Locate every Plasmodium falciparum-infected red blood cell.
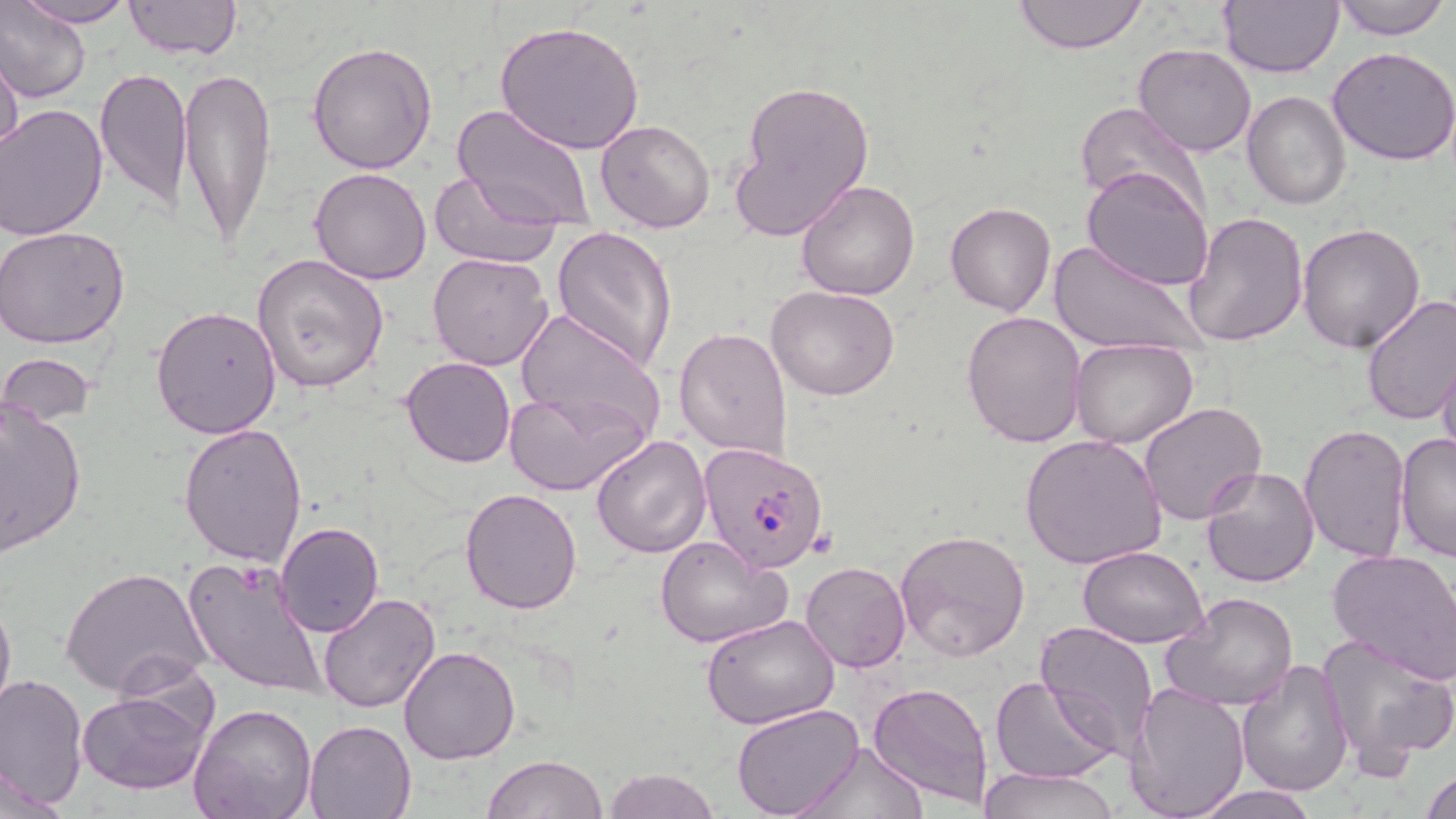
Approximate bounding boxes as [x1, y1, x2, y2] in pixels.
Plasmodium falciparum-infected red blood cells: [698, 439, 832, 572].

slide-level diagnosis = Plasmodium falciparum
modality = light microscopy
image size = 1456×819 pixels
stain = May-Grünwald-Giemsa
field of view = single
uninfected red blood cell locations = approximate bounding boxes as [x1, y1, x2, y2] in pixels: [0, 0, 91, 105], [1015, 0, 1148, 52], [1332, 0, 1451, 40], [15, 1, 136, 27], [122, 1, 243, 59], [1218, 1, 1343, 77], [495, 20, 644, 157], [308, 41, 440, 176], [1133, 42, 1256, 157], [0, 46, 23, 167], [1328, 46, 1456, 166], [178, 64, 279, 250], [95, 66, 193, 213], [729, 78, 875, 240], [1243, 91, 1351, 209], [1072, 100, 1207, 216], [452, 103, 598, 232], [1, 104, 109, 242], [595, 119, 716, 233], [310, 166, 433, 283], [1083, 167, 1214, 294], [432, 169, 563, 271], [795, 179, 922, 300], [945, 202, 1055, 317], [1182, 210, 1310, 347], [1297, 224, 1426, 352], [0, 226, 131, 348], [553, 226, 678, 370], [1047, 239, 1204, 355], [428, 252, 554, 371], [251, 254, 390, 394], [767, 284, 900, 401], [1359, 294, 1456, 425], [690, 304, 891, 427], [151, 306, 280, 438], [512, 307, 666, 444], [961, 309, 1088, 448], [674, 327, 794, 458], [1069, 337, 1199, 449], [1436, 352, 1456, 464], [0, 354, 98, 429], [400, 357, 516, 467], [504, 388, 646, 497], [0, 400, 87, 557], [1138, 402, 1268, 524], [178, 422, 307, 566], [1299, 423, 1410, 564], [1394, 431, 1456, 564], [591, 434, 711, 556], [1020, 434, 1166, 570], [1199, 464, 1322, 587], [459, 487, 583, 613], [275, 521, 385, 636], [894, 529, 1030, 661], [656, 534, 790, 649], [1077, 545, 1208, 648], [1328, 549, 1456, 684], [183, 558, 325, 695], [800, 562, 912, 673], [62, 566, 209, 701], [0, 586, 15, 724], [1165, 591, 1299, 712], [318, 594, 439, 713], [701, 614, 842, 729], [1036, 621, 1160, 760], [1315, 634, 1456, 768], [398, 646, 519, 765], [1238, 658, 1355, 797], [1, 674, 88, 807], [991, 676, 1115, 784], [867, 680, 995, 810], [1127, 682, 1251, 818], [78, 689, 210, 796], [188, 703, 317, 819], [732, 704, 865, 819], [304, 718, 417, 818], [799, 739, 927, 818], [483, 755, 606, 819], [1421, 767, 1455, 819], [603, 768, 719, 819], [975, 768, 1119, 819], [1184, 785, 1323, 818]
preparation = thin blood film
magnification = 1000x